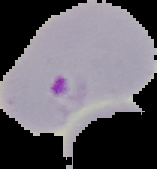

{
  "preparation": "thin blood smear",
  "image_size": "157×169 pixels",
  "result": "Plasmodium parasites detected",
  "image_type": "cell region segmented out of the field of view; surrounding area masked to black"
}